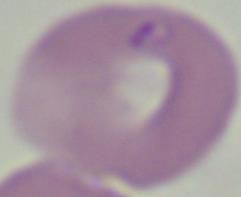
{
  "magnification": "1000x",
  "modality": "photomicrograph",
  "identification": "Babesia"
}